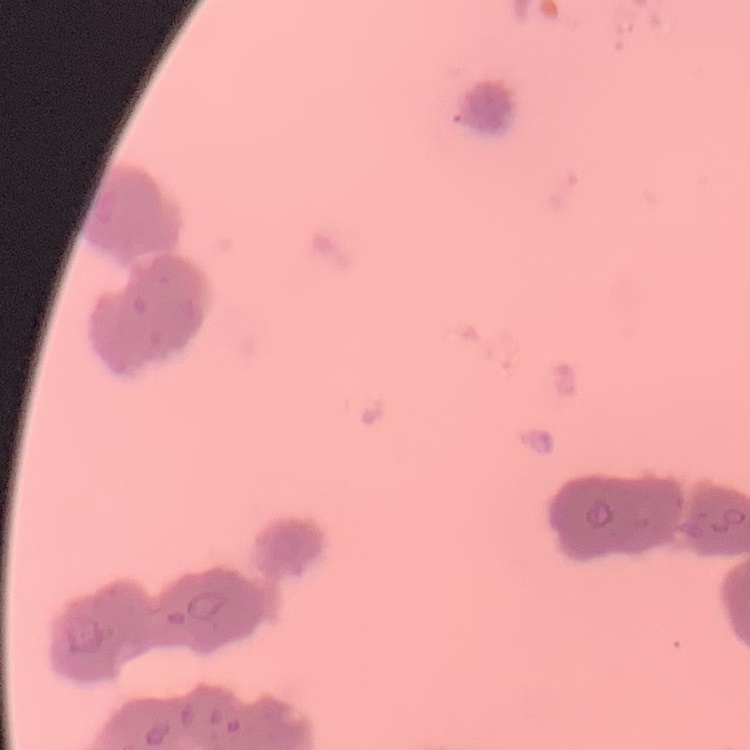
erythrocyte morphology = rouleaux formation
stain = Field's or Giemsa
preparation = thin peripheral smear
image type = one tile cut from a larger photomicrograph